Locate the cells, classifying each as a parasitized red blood cell, an uninfected red blood cell, or a white blood cell.
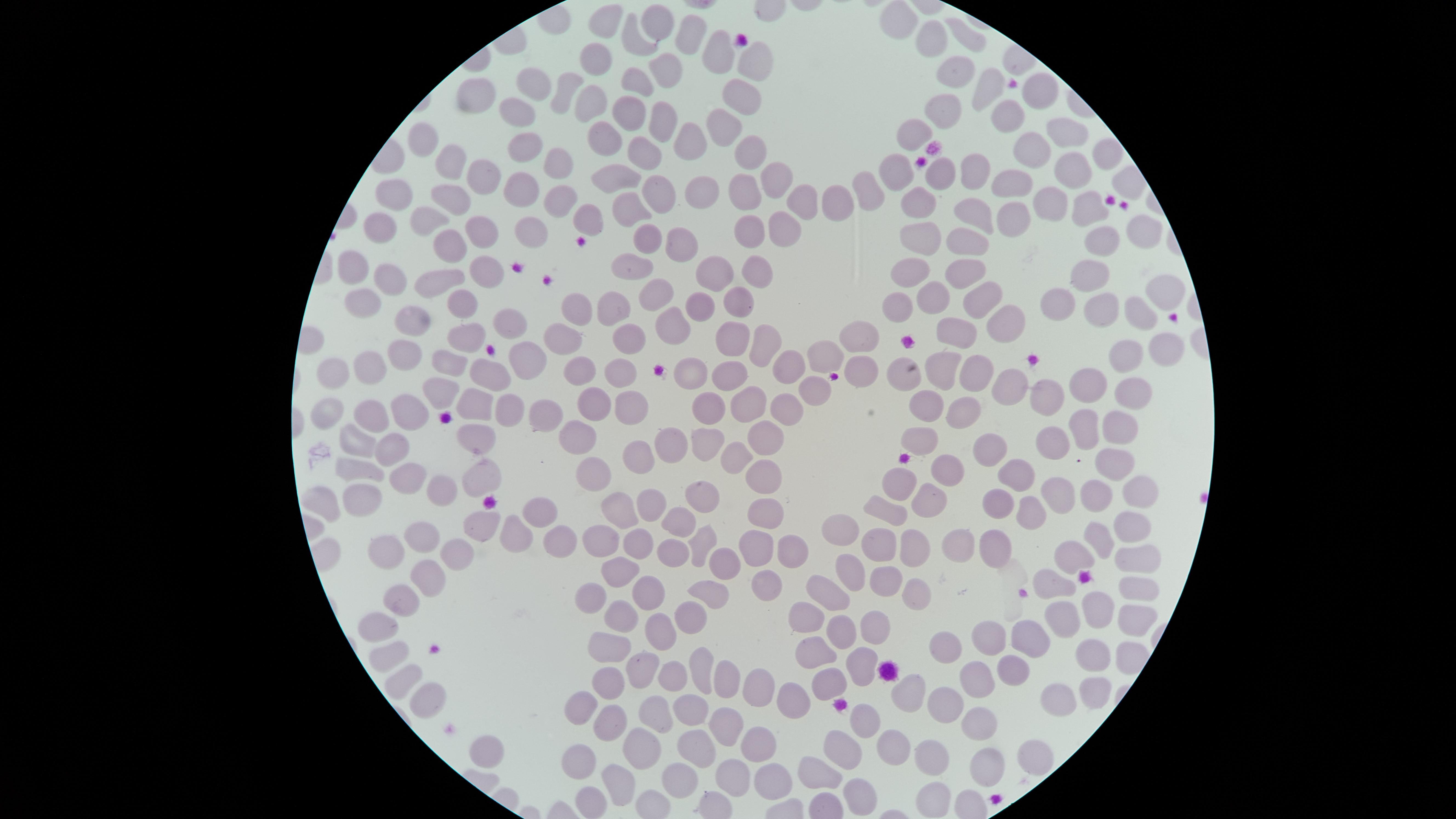
No parasitized red blood cells identified.
Approximate marker points, in pixels from the top-left corner.
Uninfected red blood cells: (x=903, y=14), (x=659, y=17), (x=605, y=21), (x=933, y=35), (x=631, y=37), (x=970, y=37), (x=692, y=38), (x=714, y=50), (x=593, y=54), (x=753, y=58), (x=659, y=67), (x=948, y=73), (x=637, y=80), (x=977, y=83), (x=530, y=85), (x=569, y=85), (x=734, y=90), (x=1032, y=90), (x=473, y=97), (x=941, y=99), (x=589, y=101), (x=518, y=110), (x=630, y=111), (x=1001, y=114), (x=661, y=119), (x=722, y=119), (x=914, y=123), (x=689, y=134), (x=1062, y=134), (x=601, y=135), (x=520, y=136), (x=424, y=138), (x=1032, y=146), (x=646, y=152), (x=755, y=153), (x=1099, y=153), (x=554, y=160), (x=978, y=161), (x=454, y=162), (x=898, y=167), (x=1076, y=167), (x=933, y=168), (x=614, y=174), (x=1012, y=176), (x=482, y=180), (x=778, y=182), (x=400, y=187), (x=520, y=187), (x=867, y=188), (x=658, y=191), (x=454, y=192), (x=698, y=192), (x=746, y=193), (x=919, y=198), (x=561, y=199), (x=1053, y=199), (x=629, y=202), (x=803, y=202), (x=835, y=202), (x=1088, y=206), (x=971, y=210), (x=593, y=216), (x=425, y=217), (x=1012, y=219), (x=782, y=223), (x=535, y=226), (x=481, y=230), (x=750, y=230), (x=1131, y=231), (x=383, y=233), (x=920, y=233), (x=677, y=236), (x=960, y=238), (x=1101, y=238), (x=649, y=239), (x=450, y=240), (x=631, y=260), (x=915, y=264), (x=755, y=265), (x=1088, y=268), (x=355, y=271), (x=484, y=271), (x=701, y=271), (x=969, y=271), (x=380, y=279), (x=440, y=280), (x=654, y=295), (x=928, y=295), (x=1157, y=295), (x=979, y=296), (x=1053, y=296), (x=735, y=298), (x=892, y=299), (x=359, y=301), (x=1100, y=303), (x=465, y=305), (x=578, y=305), (x=696, y=305), (x=608, y=306), (x=1131, y=313), (x=413, y=316), (x=671, y=321), (x=512, y=322), (x=996, y=322), (x=956, y=331), (x=556, y=333), (x=624, y=335), (x=734, y=335), (x=762, y=337), (x=863, y=338), (x=468, y=339), (x=1129, y=351), (x=1165, y=353), (x=401, y=356), (x=528, y=357), (x=827, y=361), (x=941, y=364), (x=374, y=365), (x=447, y=365), (x=791, y=365), (x=730, y=370), (x=339, y=371), (x=583, y=371), (x=621, y=371), (x=861, y=371), (x=492, y=372), (x=691, y=372), (x=964, y=375), (x=900, y=376), (x=1092, y=376), (x=1009, y=386), (x=812, y=389), (x=1132, y=389), (x=1056, y=390), (x=441, y=392), (x=627, y=402), (x=924, y=402), (x=472, y=403), (x=752, y=403), (x=592, y=404), (x=409, y=405), (x=505, y=406), (x=961, y=406), (x=331, y=408), (x=708, y=408), (x=787, y=408), (x=372, y=410), (x=542, y=413), (x=1113, y=422), (x=1081, y=424), (x=1053, y=434), (x=582, y=435), (x=769, y=435), (x=477, y=438), (x=704, y=441), (x=923, y=441), (x=357, y=442), (x=673, y=443), (x=985, y=447), (x=391, y=450), (x=637, y=452), (x=742, y=457), (x=1113, y=459), (x=597, y=465), (x=357, y=466), (x=945, y=467), (x=1020, y=468), (x=762, y=473), (x=478, y=475), (x=407, y=478), (x=895, y=478), (x=1057, y=489), (x=1096, y=489), (x=439, y=490), (x=1139, y=491), (x=923, y=495), (x=999, y=498), (x=653, y=500), (x=322, y=503), (x=695, y=503), (x=370, y=504), (x=618, y=506), (x=881, y=511), (x=1027, y=511), (x=537, y=512), (x=760, y=515), (x=679, y=522), (x=480, y=524), (x=1129, y=527), (x=842, y=528), (x=604, y=535), (x=513, y=536), (x=1098, y=536), (x=424, y=537), (x=698, y=538), (x=994, y=538), (x=957, y=540), (x=552, y=541), (x=639, y=543), (x=880, y=544), (x=786, y=546), (x=913, y=546), (x=671, y=547), (x=399, y=551), (x=1082, y=556), (x=1134, y=556), (x=753, y=559), (x=459, y=561), (x=728, y=564), (x=622, y=567), (x=854, y=571), (x=886, y=578), (x=426, y=580), (x=769, y=580), (x=1053, y=581), (x=1136, y=587), (x=593, y=589), (x=834, y=589), (x=718, y=591), (x=649, y=592), (x=912, y=593), (x=402, y=602), (x=1096, y=607), (x=623, y=614), (x=697, y=615), (x=807, y=615), (x=1065, y=615), (x=1130, y=617), (x=382, y=624), (x=842, y=625), (x=874, y=625), (x=666, y=628), (x=991, y=632), (x=1034, y=632), (x=608, y=640), (x=945, y=646), (x=819, y=649), (x=1090, y=653), (x=391, y=654), (x=859, y=659), (x=703, y=660), (x=640, y=665), (x=1011, y=666), (x=673, y=668), (x=727, y=674), (x=399, y=680), (x=971, y=680), (x=828, y=683), (x=606, y=684), (x=757, y=688), (x=1093, y=692), (x=911, y=694), (x=946, y=696), (x=584, y=697), (x=423, y=698), (x=1056, y=700), (x=785, y=701), (x=655, y=705), (x=692, y=709), (x=976, y=715), (x=730, y=718), (x=860, y=724), (x=612, y=726), (x=641, y=743), (x=692, y=744), (x=889, y=744), (x=767, y=745), (x=487, y=748), (x=1035, y=749), (x=836, y=751), (x=932, y=756), (x=987, y=763), (x=580, y=765), (x=817, y=769), (x=681, y=771), (x=776, y=777), (x=729, y=781), (x=620, y=785), (x=849, y=793), (x=592, y=801), (x=932, y=801).
No white blood cells identified.

Summary:
  - Preparation: thin smear of blood
  - Capture: smartphone photograph through the microscope eyepiece
  - Stain: Giemsa
  - Visible region: circular
  - Field of view: single
  - Image size: 1456×819 pixels